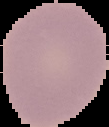
Cell region segmented out of the field of view; the surrounding area is masked to black. From a thin blood smear. Image is 109×127 pixels. Malaria status: uninfected.